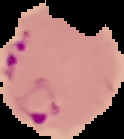
Result: Plasmodium parasites detected. Image is 124×139 pixels. Cell region segmented out of the field of view; the surrounding area is masked to black. From a thin blood smear.